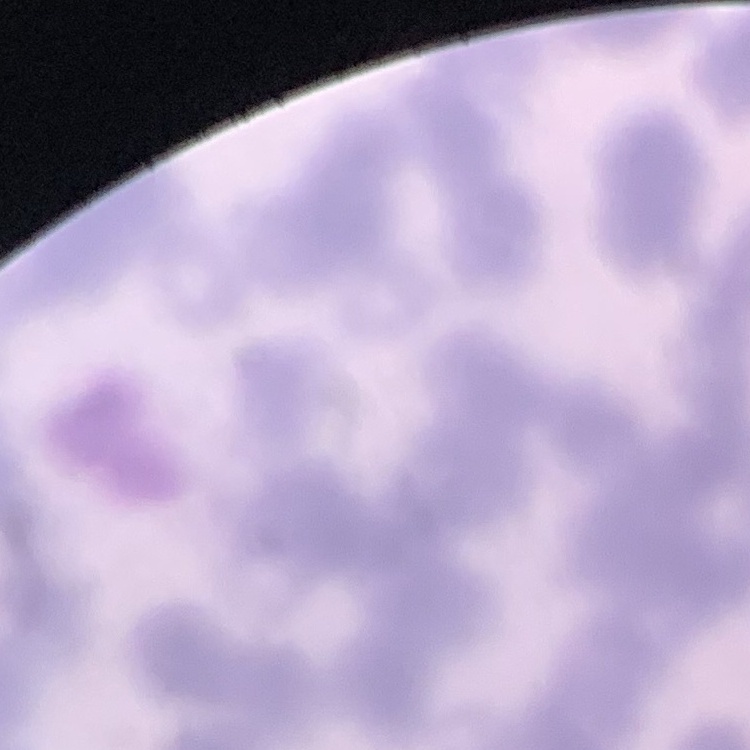
Summary:
  - Red blood cell morphology: rouleaux formation
  - Image type: one tile cut from a larger photomicrograph
  - Preparation: thin peripheral smear
  - Stain: Field's or Giemsa